Classify this cell by malaria status.
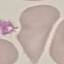

Uninfected.

Thin blood smear. Cell patch, automatically extracted from a larger field of view and resized to 64 × 64 pixels. Giemsa stain. Photographed with a smartphone camera at the microscope eyepiece.